Give the extent of all uninfected red blood cells.
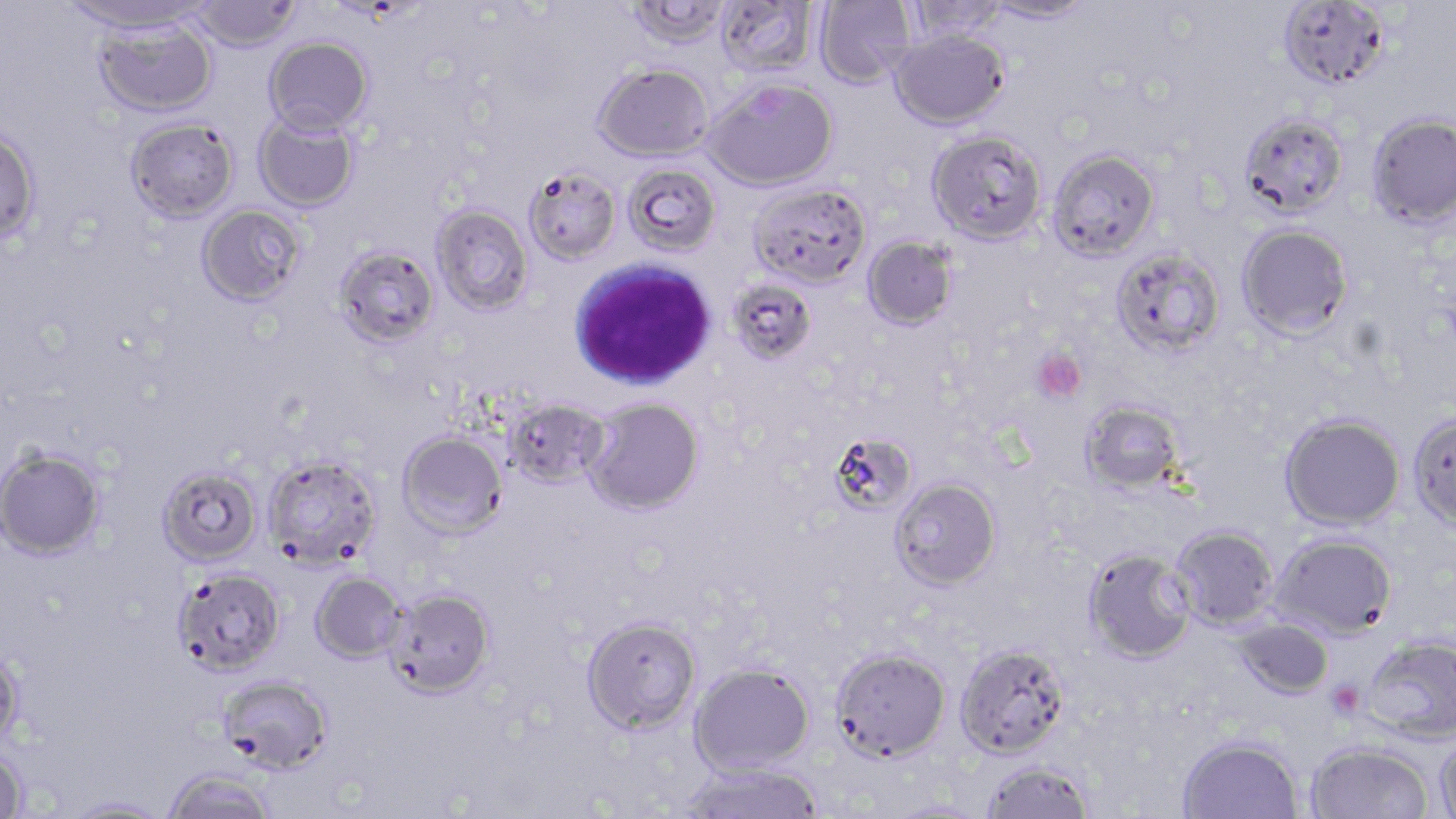
Approximate bounding boxes as named x1/y1/x2/y2 corners in pixels.
Uninfected red blood cells: (x1=63, y1=0, x2=209, y2=35), (x1=715, y1=0, x2=819, y2=78), (x1=814, y1=0, x2=915, y2=88), (x1=980, y1=0, x2=1097, y2=24), (x1=1277, y1=0, x2=1392, y2=90), (x1=188, y1=1, x2=302, y2=52), (x1=626, y1=1, x2=731, y2=49), (x1=903, y1=1, x2=1009, y2=42), (x1=93, y1=17, x2=218, y2=118), (x1=889, y1=28, x2=1009, y2=129), (x1=264, y1=36, x2=373, y2=136), (x1=593, y1=63, x2=713, y2=161), (x1=704, y1=78, x2=837, y2=190), (x1=253, y1=112, x2=359, y2=212), (x1=1239, y1=112, x2=1348, y2=217), (x1=1366, y1=112, x2=1456, y2=228), (x1=126, y1=117, x2=239, y2=223), (x1=0, y1=127, x2=41, y2=245), (x1=926, y1=130, x2=1047, y2=244), (x1=1048, y1=149, x2=1160, y2=260), (x1=623, y1=163, x2=721, y2=257), (x1=523, y1=166, x2=621, y2=264), (x1=749, y1=183, x2=871, y2=288), (x1=197, y1=204, x2=306, y2=306), (x1=431, y1=204, x2=533, y2=315), (x1=1237, y1=223, x2=1353, y2=340), (x1=863, y1=236, x2=957, y2=330), (x1=333, y1=244, x2=440, y2=349), (x1=1111, y1=246, x2=1227, y2=359), (x1=727, y1=278, x2=817, y2=365), (x1=502, y1=397, x2=610, y2=488), (x1=583, y1=397, x2=704, y2=515), (x1=1080, y1=399, x2=1186, y2=495), (x1=1407, y1=412, x2=1456, y2=531), (x1=1280, y1=413, x2=1405, y2=530), (x1=397, y1=430, x2=508, y2=539), (x1=833, y1=430, x2=916, y2=511), (x1=1, y1=447, x2=106, y2=560), (x1=263, y1=454, x2=382, y2=569), (x1=157, y1=465, x2=262, y2=566), (x1=890, y1=477, x2=1002, y2=589), (x1=1169, y1=525, x2=1278, y2=630), (x1=1270, y1=533, x2=1397, y2=638), (x1=1083, y1=547, x2=1197, y2=663), (x1=173, y1=566, x2=285, y2=675), (x1=311, y1=572, x2=405, y2=663), (x1=385, y1=588, x2=494, y2=698), (x1=581, y1=616, x2=701, y2=734), (x1=1233, y1=618, x2=1334, y2=698), (x1=1363, y1=634, x2=1456, y2=743), (x1=955, y1=642, x2=1070, y2=758), (x1=0, y1=645, x2=26, y2=750), (x1=830, y1=646, x2=951, y2=760), (x1=689, y1=663, x2=814, y2=775), (x1=217, y1=674, x2=333, y2=774), (x1=1435, y1=734, x2=1456, y2=819), (x1=1178, y1=736, x2=1303, y2=819), (x1=1306, y1=742, x2=1433, y2=819), (x1=0, y1=747, x2=28, y2=818), (x1=981, y1=760, x2=1095, y2=819), (x1=681, y1=762, x2=823, y2=819), (x1=163, y1=769, x2=276, y2=819), (x1=62, y1=796, x2=173, y2=817), (x1=883, y1=799, x2=991, y2=818).

slide-level diagnosis = Plasmodium falciparum
stain = May-Grünwald-Giemsa
platelet locations = approximate bounding boxes as named x1/y1/x2/y2 corners in pixels: (x1=1032, y1=348, x2=1087, y2=402), (x1=1326, y1=680, x2=1365, y2=719)
preparation = thin blood smear
white blood cell locations = approximate bounding boxes as named x1/y1/x2/y2 corners in pixels: (x1=568, y1=259, x2=717, y2=391)
modality = light microscopy
magnification = 1000x
image size = 1456×819 pixels
field of view = one of a larger specimen